Locate and identify every blood parasite.
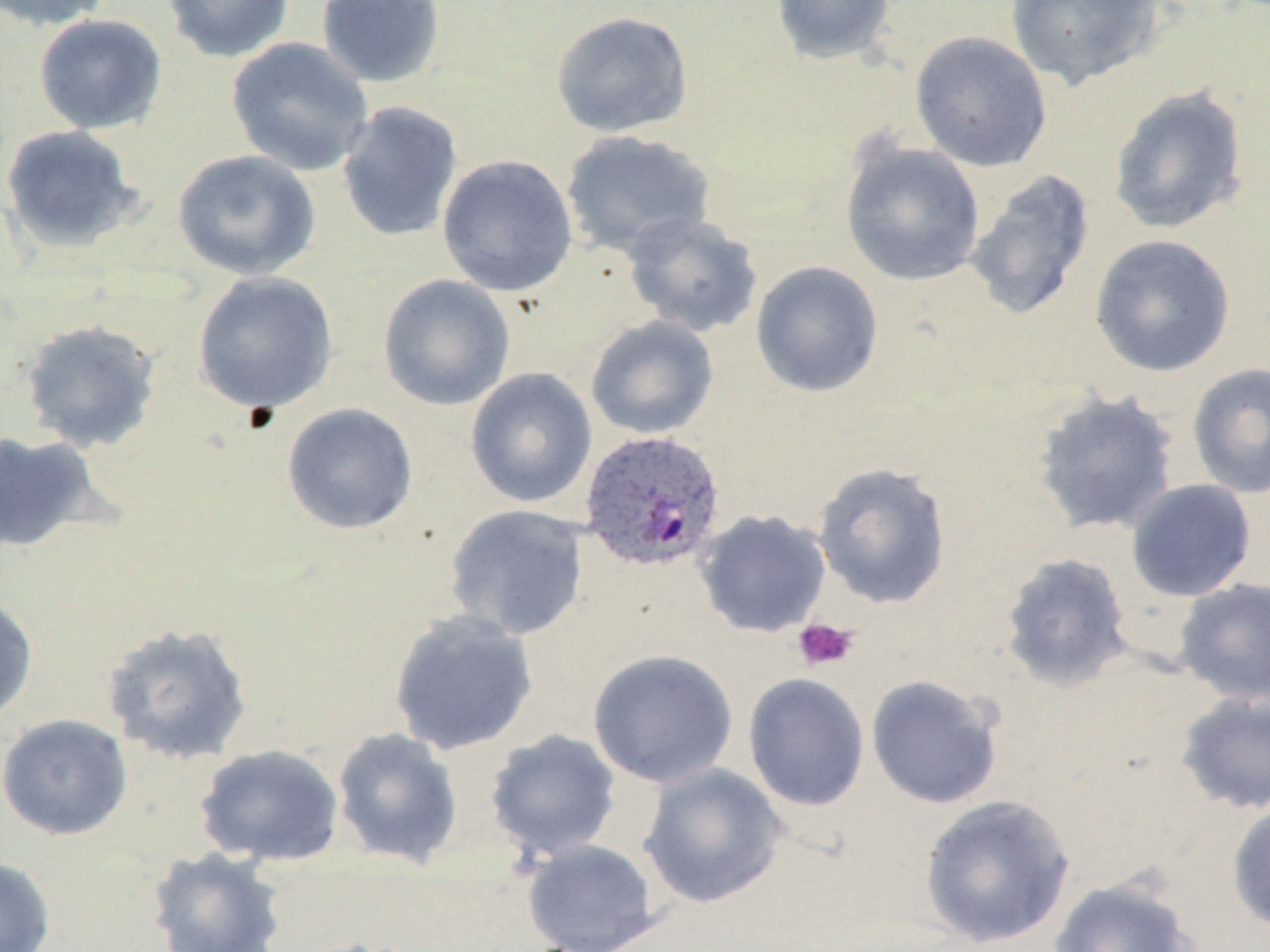

Approximate bounding boxes as (x1,y1)-(x2,y2) corner pairs in pixels.
Plasmodium ovale-infected red blood cells: (578,429)-(727,572).
No Plasmodium falciparum, Plasmodium malariae, Plasmodium vivax, Babesia divergens, or Trypanosoma brucei observed.

slide_level_diagnosis: Plasmodium ovale
field_of_view: single
preparation: thin blood smear
uninfected_red_blood_cell_locations: 'approximate bounding boxes as (x1,y1)-(x2,y2) corner pairs in pixels: (0,0)-(116,31), (162,0)-(295,63), (316,0)-(445,88), (769,0)-(897,65), (1005,0)-(1166,92), (551,10)-(694,138), (33,14)-(167,135), (909,30)-(1053,172), (225,36)-(374,176), (1108,85)-(1250,236), (335,100)-(464,243), (0,125)-(145,254), (560,130)-(716,260), (840,139)-(985,286), (172,149)-(321,280), (437,154)-(578,297), (964,169)-(1096,322), (622,212)-(764,338), (1090,234)-(1236,377), (751,261)-(884,398), (191,271)-(340,415), (377,273)-(516,411), (585,315)-(719,439), (18,319)-(162,452), (1186,362)-(1270,499), (464,367)-(597,508), (1030,390)-(1182,537), (281,402)-(419,535), (0,430)-(105,554), (813,461)-(952,609), (1125,479)-(1257,602), (443,503)-(590,641), (695,509)-(832,638), (1000,552)-(1134,692), (1173,577)-(1270,706), (0,590)-(38,726), (388,609)-(539,756), (100,621)-(254,767), (586,648)-(739,788), (742,672)-(870,812), (866,674)-(1005,809), (1175,689)-(1270,814), (0,713)-(133,840), (331,727)-(464,869), (485,729)-(621,861), (194,743)-(345,868), (639,763)-(788,908), (918,794)-(1076,948), (1226,798)-(1270,936), (522,839)-(662,952), (147,846)-(287,952), (0,856)-(56,952), (1047,877)-(1199,952)'
image_size: 1270×952 pixels
modality: light microscopy
platelet_locations: 'approximate bounding boxes as (x1,y1)-(x2,y2) corner pairs in pixels: (793,618)-(858,671)'
magnification: 1000x
stain: May-Grünwald-Giemsa